Report the malaria status of this cell.
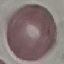

Uninfected.

stain = Giemsa
capture = smartphone through the microscope eyepiece
preparation = thin blood film
image type = automatically extracted cell patch, resized to 64 × 64 pixels